Name the cell type shown.
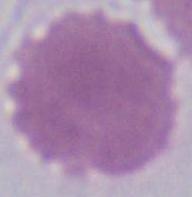
An erythrocyte.

magnification: 1000x
modality: micrograph